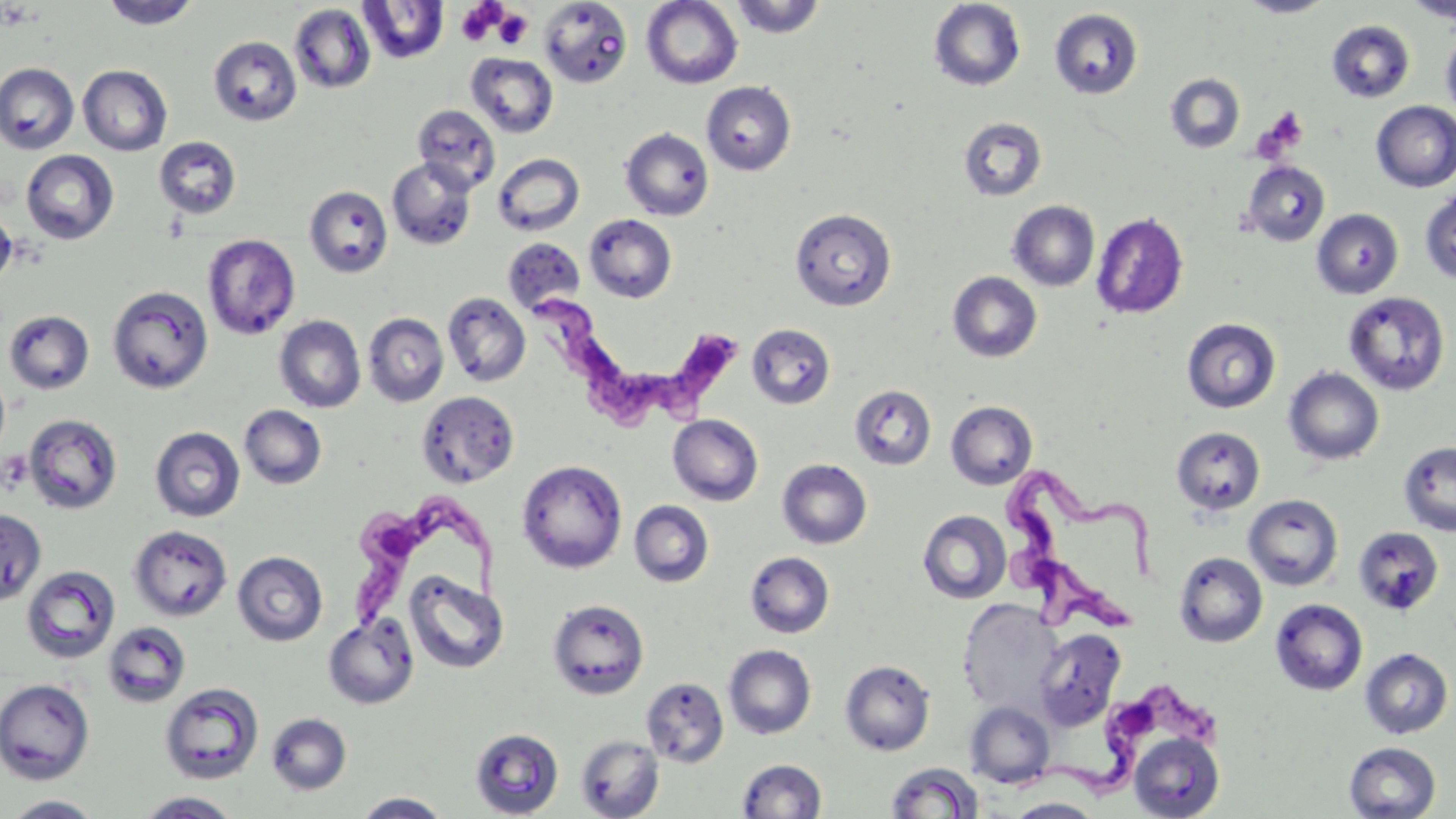
slide-level diagnosis = Trypanosoma brucei
platelet locations = approximate bounding boxes as [x1, y1, x2, y2] in pixels: [457, 2, 500, 45], [493, 9, 532, 50], [1254, 109, 1308, 160]
preparation = thin blood film
image size = 1456×819 pixels
magnification = 1000x
modality = optical microscopy
uninfected red blood cell locations = approximate bounding boxes as [x1, y1, x2, y2] in pixels: [729, 0, 827, 38], [928, 0, 1026, 91], [1237, 0, 1337, 18], [1406, 0, 1456, 25], [100, 1, 202, 30], [358, 1, 448, 64], [538, 1, 632, 88], [641, 1, 743, 88], [289, 4, 376, 94], [1050, 8, 1144, 100], [1327, 20, 1416, 103], [1440, 31, 1456, 123], [208, 35, 302, 126], [465, 53, 558, 138], [0, 62, 79, 155], [78, 65, 173, 156], [1165, 73, 1245, 154], [702, 81, 796, 176], [1371, 101, 1456, 192], [412, 104, 500, 193], [958, 116, 1047, 201], [620, 128, 713, 220], [153, 136, 241, 220], [20, 149, 119, 244], [492, 153, 585, 236], [386, 157, 477, 250], [1241, 161, 1330, 246], [304, 185, 393, 278], [1419, 189, 1456, 285], [1008, 200, 1099, 291], [0, 206, 16, 288], [789, 208, 896, 311], [1311, 208, 1404, 298], [1091, 212, 1189, 320], [584, 214, 676, 303], [202, 233, 301, 340], [502, 236, 586, 315], [948, 271, 1042, 362], [107, 285, 214, 394], [1343, 291, 1450, 396], [442, 292, 531, 387], [3, 310, 94, 395], [363, 313, 448, 406], [274, 315, 365, 412], [1181, 318, 1281, 413], [747, 323, 836, 410], [0, 365, 10, 462], [1284, 367, 1384, 465], [850, 386, 936, 470], [417, 391, 518, 488], [946, 401, 1037, 489], [239, 404, 327, 490], [23, 414, 123, 514], [668, 415, 763, 505], [150, 426, 245, 522], [1171, 426, 1265, 516], [1398, 440, 1456, 537], [777, 459, 872, 548], [517, 460, 627, 574], [1243, 494, 1343, 590], [629, 500, 714, 587], [0, 509, 46, 605], [918, 510, 1012, 603], [128, 525, 232, 621], [1353, 526, 1444, 616], [232, 551, 328, 646], [745, 551, 835, 638], [1173, 551, 1267, 648], [22, 565, 120, 663], [405, 570, 509, 674], [958, 598, 1063, 716], [548, 599, 649, 700], [1270, 599, 1368, 695], [323, 614, 419, 709], [102, 620, 191, 707], [1034, 629, 1126, 731], [724, 644, 816, 739], [1360, 648, 1453, 739], [840, 660, 935, 756], [641, 677, 729, 768], [0, 679, 95, 784], [160, 683, 264, 784], [965, 701, 1055, 788], [266, 713, 352, 795], [470, 727, 564, 818], [1128, 732, 1225, 819], [575, 735, 664, 819], [1343, 741, 1441, 819], [736, 759, 827, 818], [885, 762, 984, 818], [135, 791, 242, 818], [353, 792, 451, 818], [3, 795, 105, 818], [1008, 798, 1103, 818]
field of view = single
stain = May-Grünwald-Giemsa
Trypanosoma brucei locations = approximate bounding boxes as [x1, y1, x2, y2] in pixels: [534, 289, 756, 436], [1001, 471, 1164, 637], [357, 495, 505, 627], [1012, 690, 1227, 805]